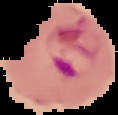

The area outside the segmented cell region is set to black. Malaria status: parasitized. From a thin blood film. Image is 118×115 pixels.